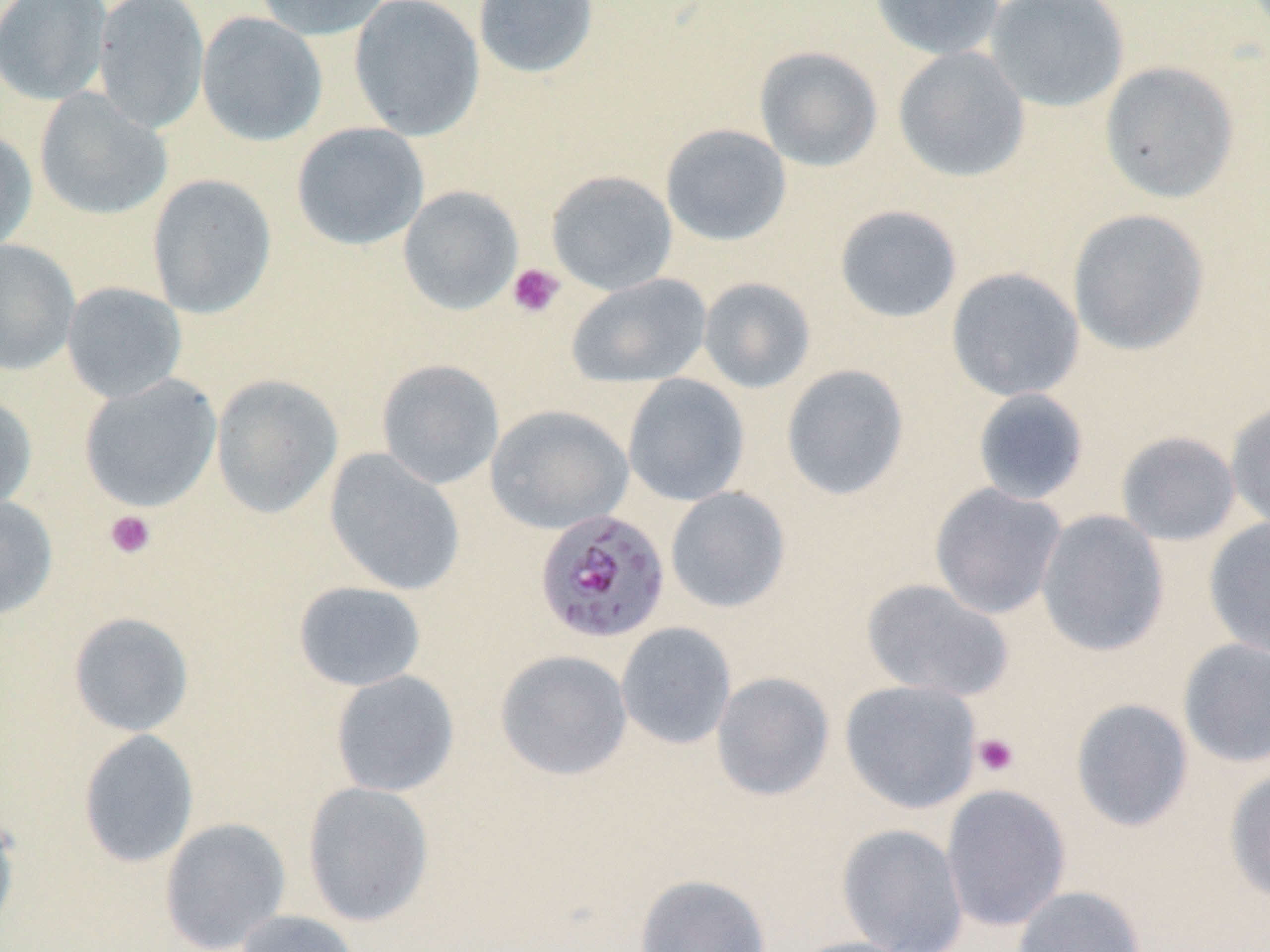
Summary:
  - Coordinate format: approximate bounding boxes as [x1, y1, x2, y2] in pixels
  - Plasmodium falciparum-infected red blood cell locations: [534, 508, 671, 644]
  - Uninfected red blood cell locations: [0, 0, 112, 106], [93, 0, 209, 134], [253, 0, 392, 40], [349, 0, 485, 141], [473, 0, 599, 79], [870, 0, 1006, 61], [984, 0, 1129, 112], [196, 11, 327, 147], [754, 45, 883, 172], [892, 46, 1030, 183], [1099, 61, 1240, 203], [34, 89, 172, 221], [291, 122, 429, 251], [660, 123, 792, 246], [0, 127, 37, 254], [546, 170, 678, 295], [146, 173, 278, 320], [398, 185, 523, 315], [834, 205, 963, 324], [1067, 208, 1210, 356], [0, 239, 80, 376], [946, 267, 1084, 403], [566, 273, 712, 387], [698, 277, 816, 393], [61, 282, 187, 403], [376, 359, 505, 490], [780, 363, 910, 502], [79, 374, 222, 512], [211, 374, 343, 518], [622, 374, 749, 506], [972, 388, 1090, 505], [0, 392, 37, 515], [1225, 399, 1270, 533], [486, 404, 633, 535], [1116, 431, 1241, 546], [324, 449, 466, 596], [929, 483, 1067, 619], [665, 486, 791, 613], [0, 495, 58, 620], [1035, 510, 1169, 657], [1203, 517, 1270, 658], [862, 578, 1013, 702], [292, 581, 426, 691], [68, 612, 194, 737], [616, 622, 736, 750], [1177, 637, 1270, 768], [494, 649, 633, 781], [330, 670, 460, 797], [711, 671, 834, 801], [839, 679, 982, 814], [1070, 698, 1194, 833], [78, 728, 199, 868], [1224, 767, 1270, 904], [302, 780, 434, 927], [941, 784, 1072, 931], [0, 807, 21, 939], [159, 817, 291, 952], [837, 823, 968, 952], [634, 873, 772, 952], [1011, 885, 1146, 951], [235, 910, 360, 952], [787, 936, 920, 952]
  - Platelet locations: [506, 263, 565, 318], [104, 510, 156, 559], [972, 732, 1020, 778]
  - Slide-level diagnosis: Plasmodium falciparum
  - Modality: optical microscopy
  - Image size: 1270×952 pixels
  - Magnification: 1000x
  - Field of view: one of a larger specimen
  - Stain: May-Grünwald-Giemsa
  - Preparation: thin blood film